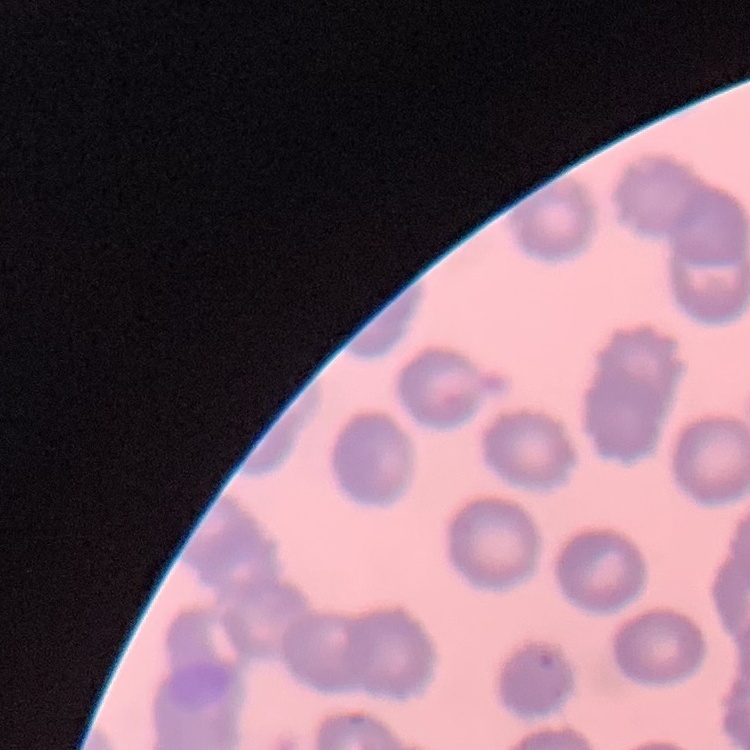 The red blood cells exhibit no rouleaux formation. One tile cut from a larger photomicrograph. Field's or Giemsa stain. Thin blood film.